Report the malaria status of this cell.
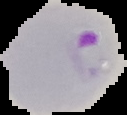

It is parasitized.

image type = cell region segmented out of the field of view; surrounding area masked to black
image size = 127×115 pixels
preparation = thin blood smear